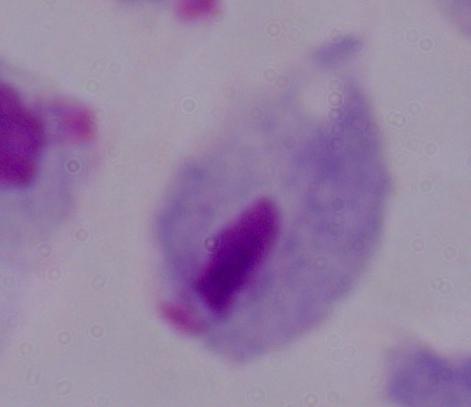

{
  "magnification": "1000x",
  "modality": "micrograph",
  "identification": "trichomonad"
}